State the blood parasite species.
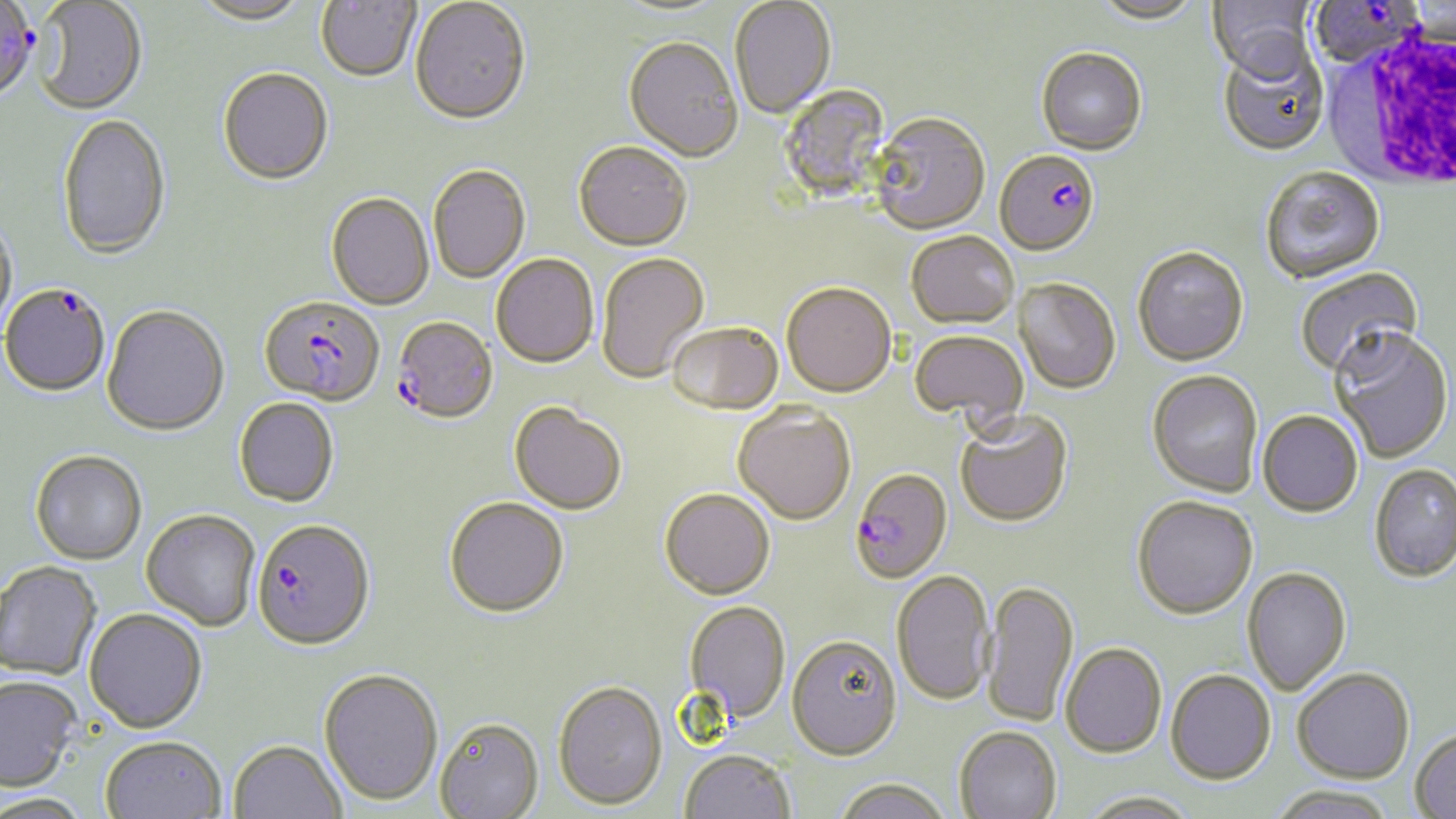
Plasmodium falciparum.

preparation: thin blood smear
plasmodium_falciparum_infected_red_blood_cell_locations: 'approximate bounding boxes as [x1, y1, x2, y2] in pixels: [1309, 0, 1425, 69], [0, 4, 42, 105], [994, 151, 1100, 258], [2, 282, 111, 397], [260, 297, 385, 407], [392, 318, 498, 427], [850, 470, 953, 585], [252, 521, 376, 654]'
white_blood_cell_locations: 'approximate bounding boxes as [x1, y1, x2, y2] in pixels: [1328, 28, 1455, 193]'
magnification: 1000x
modality: optical microscopy
uninfected_red_blood_cell_locations: 'approximate bounding boxes as [x1, y1, x2, y2] in pixels: [191, 0, 313, 27], [315, 0, 421, 84], [730, 0, 836, 120], [1090, 0, 1205, 26], [1208, 0, 1318, 83], [32, 1, 148, 114], [410, 1, 531, 128], [611, 1, 731, 20], [623, 39, 742, 164], [1217, 44, 1330, 157], [1036, 49, 1147, 157], [217, 69, 334, 186], [776, 84, 894, 203], [57, 113, 171, 259], [868, 115, 990, 237], [573, 143, 693, 253], [428, 166, 531, 284], [1260, 168, 1386, 285], [326, 194, 435, 311], [0, 212, 18, 340], [906, 233, 1019, 330], [1132, 248, 1249, 368], [596, 253, 710, 384], [491, 255, 599, 369], [1295, 266, 1424, 380], [1013, 279, 1121, 395], [781, 285, 897, 400], [102, 305, 229, 436], [666, 325, 783, 417], [1329, 328, 1453, 463], [909, 331, 1028, 424], [1147, 370, 1263, 498], [234, 399, 339, 509], [509, 404, 626, 517], [733, 406, 856, 527], [955, 410, 1074, 529], [1257, 410, 1363, 517], [30, 451, 147, 564], [1369, 463, 1456, 584], [660, 490, 775, 601], [1132, 496, 1258, 621], [444, 499, 569, 620], [142, 510, 261, 632], [0, 561, 101, 680], [1242, 567, 1352, 696], [891, 571, 995, 707], [981, 582, 1079, 729], [684, 601, 790, 724], [84, 610, 207, 735], [786, 636, 903, 763], [1061, 644, 1167, 760], [318, 669, 443, 807], [1292, 669, 1414, 784], [1165, 671, 1275, 787], [0, 677, 82, 793], [553, 681, 667, 811], [434, 719, 545, 819], [954, 727, 1062, 819], [1411, 728, 1456, 817], [100, 738, 226, 819], [228, 741, 346, 819], [679, 751, 795, 819], [834, 779, 951, 819], [1267, 786, 1398, 819], [1078, 794, 1201, 819], [0, 795, 95, 819]'
stain: May-Grünwald-Giemsa
field_of_view: single
image_size: 1456×819 pixels